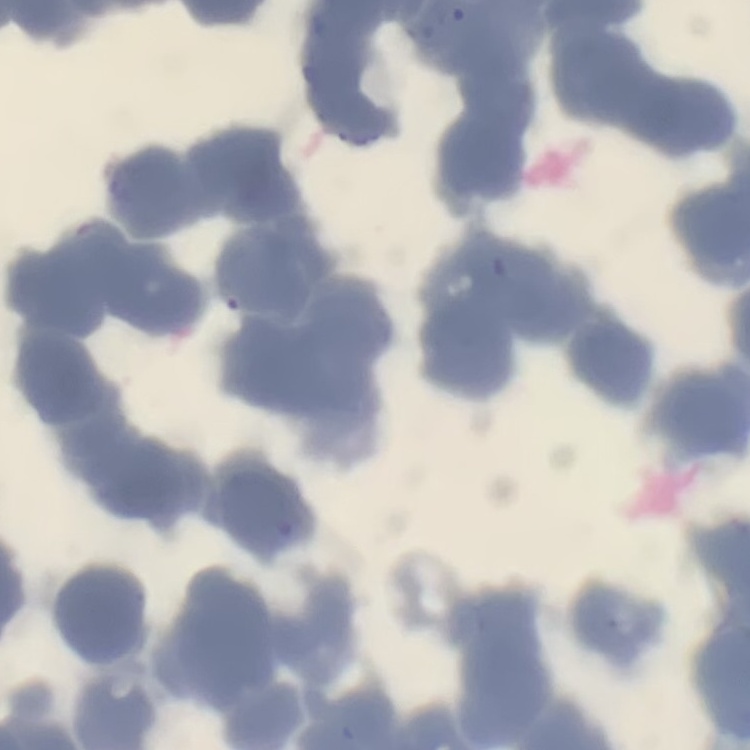

{
  "red_blood_cell_morphology": "rouleaux formation",
  "image_type": "square crop of a larger photomicrograph",
  "preparation": "thin blood smear",
  "stain": "Field's or Giemsa"
}